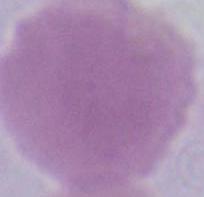
Summary:
  - Identification: erythrocyte
  - Magnification: 1000x
  - Modality: photomicrograph